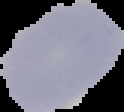

image type = segmented cell region with the area outside set to black
image size = 124×112 pixels
malaria status = uninfected
preparation = thin blood film